Report the malaria status of this cell.
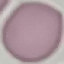

It is uninfected.

Summary:
  - Capture: smartphone camera at the microscope eyepiece
  - Image type: cell patch, automatically extracted from a larger field of view and resized to 64 × 64 pixels
  - Stain: Giemsa
  - Preparation: thin blood film